Point out each Plasmodium parasite.
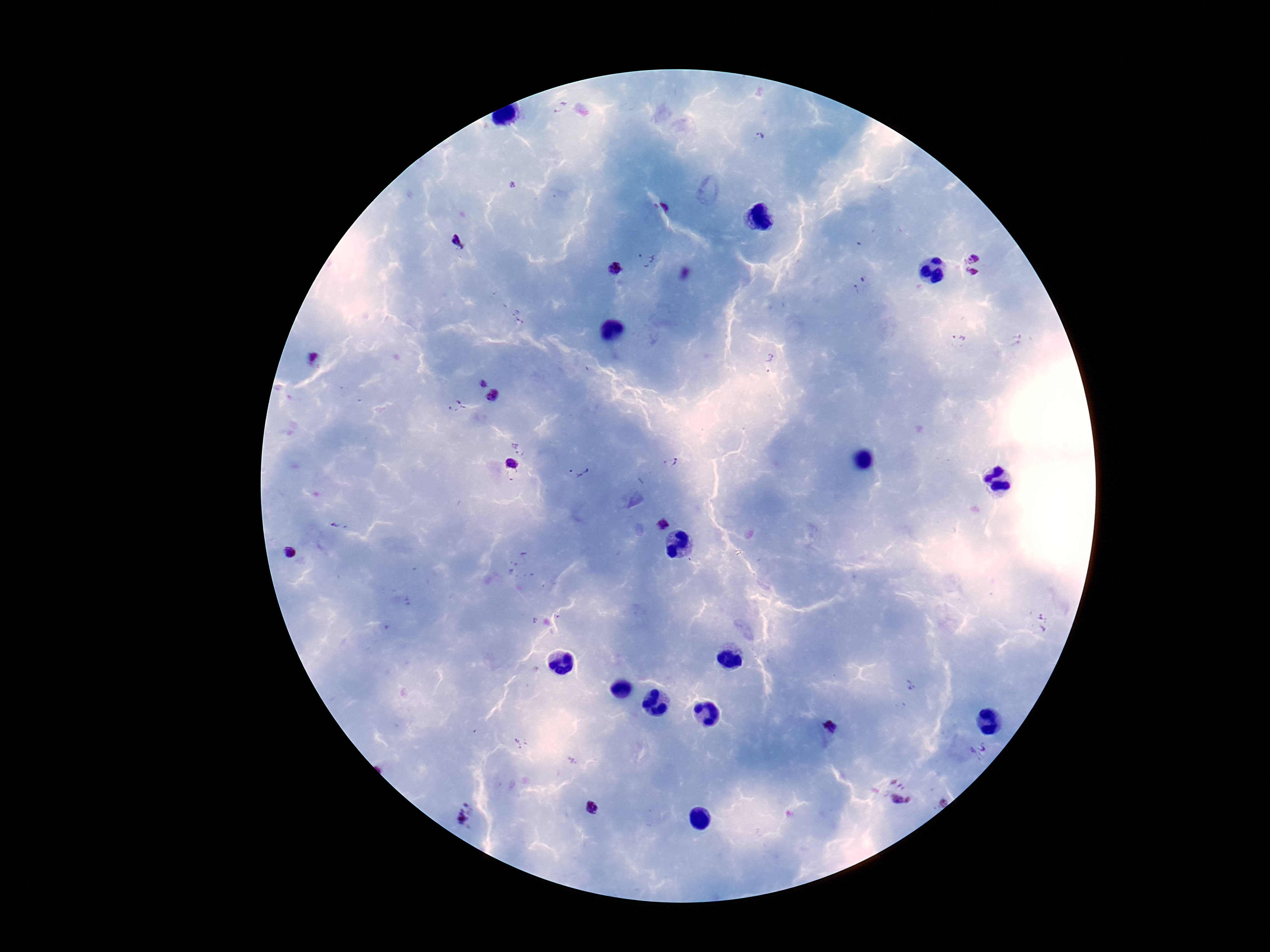
Approximate centers as {x, y} in pixels.
Plasmodium parasites: {759, 136}, {668, 206}, {460, 243}, {974, 258}, {646, 260}, {615, 271}, {971, 273}, {864, 279}, {856, 290}, {959, 341}, {312, 357}, {768, 362}, {484, 384}, {492, 396}, {457, 406}, {671, 462}, {512, 463}, {579, 471}, {511, 477}, {663, 525}, {338, 526}, {289, 553}, {557, 617}, {1043, 623}, {911, 686}, {830, 726}, {521, 743}, {977, 750}, {899, 783}, {901, 801}, {942, 802}, {592, 808}, {465, 816}.

One field from this slide. Patient malaria status: positive. Image is 1270×952 pixels. 100x magnification. Giemsa-stained preparation. Thick blood film. Smartphone photograph taken through the microscope eyepiece.